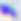
Summary:
  - Modality: photomicrograph
  - Identification: Toxoplasma gondii
  - Magnification: 400x